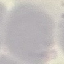

malaria_status: uninfected
preparation: thin blood film
stain: Giemsa
image_type: cell patch, automatically extracted from a larger field of view and resized to 64 × 64 pixels
capture: smartphone camera at the microscope eyepiece